Give the position of every Plasmodium parasite visible.
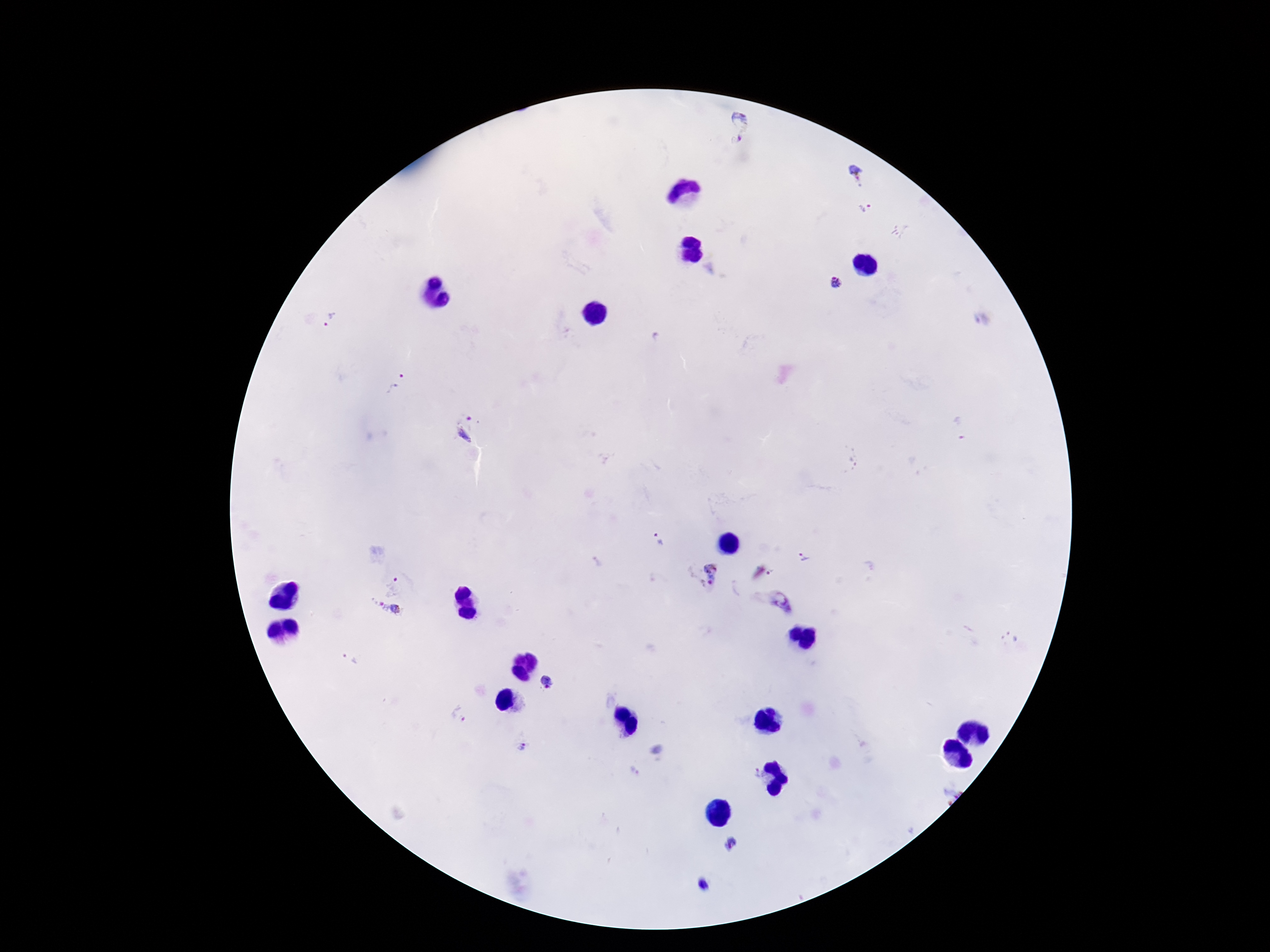
Approximate centers as [x, y] in pixels.
Plasmodium parasites: [740, 118], [737, 141], [855, 175], [867, 210], [838, 285], [330, 320], [983, 320], [399, 386], [959, 429], [466, 431], [659, 540], [802, 558], [700, 574], [773, 575], [393, 586], [782, 603], [379, 605], [396, 609], [351, 657], [546, 683], [460, 716], [521, 746], [634, 771], [752, 772], [729, 845], [703, 884].

Summary:
  - Capture: smartphone camera through the microscope eyepiece
  - Magnification: 100x
  - Field of view: single
  - Image size: 1270×952 pixels
  - Stain: Giemsa
  - Patient malaria status: positive
  - Preparation: thick blood film